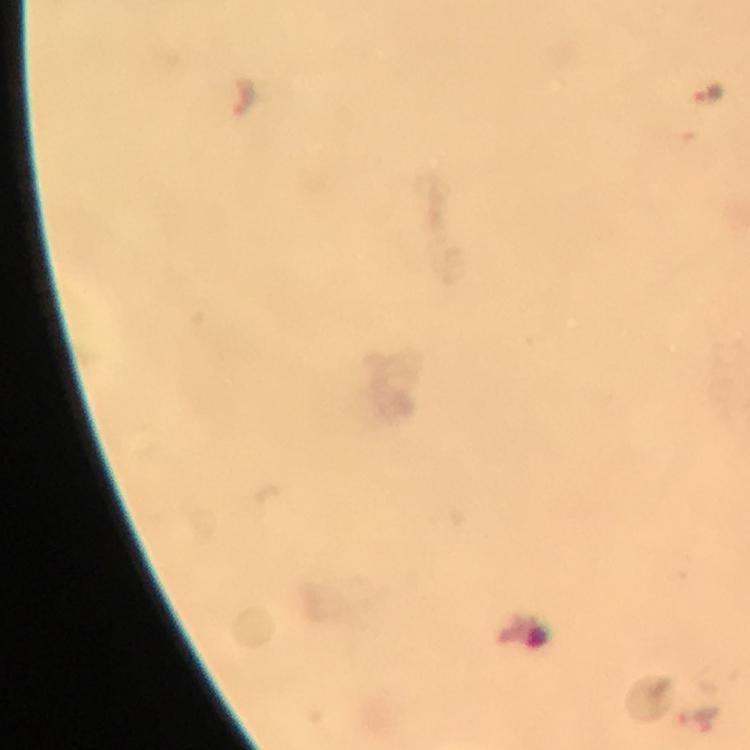

image_size: 750×750 pixels
malaria_parasite_locations: 'approximate centers as (x, y) in pixels: (707, 91), (244, 95), (697, 716)'
immersion_oil: used
magnification: 100x
cropped_from: one field of view
stain: Giemsa
context: from a malaria diagnostic workup
preparation: thick blood film
capture: smartphone mounted on the microscope